Assess the morphology of the erythrocytes.
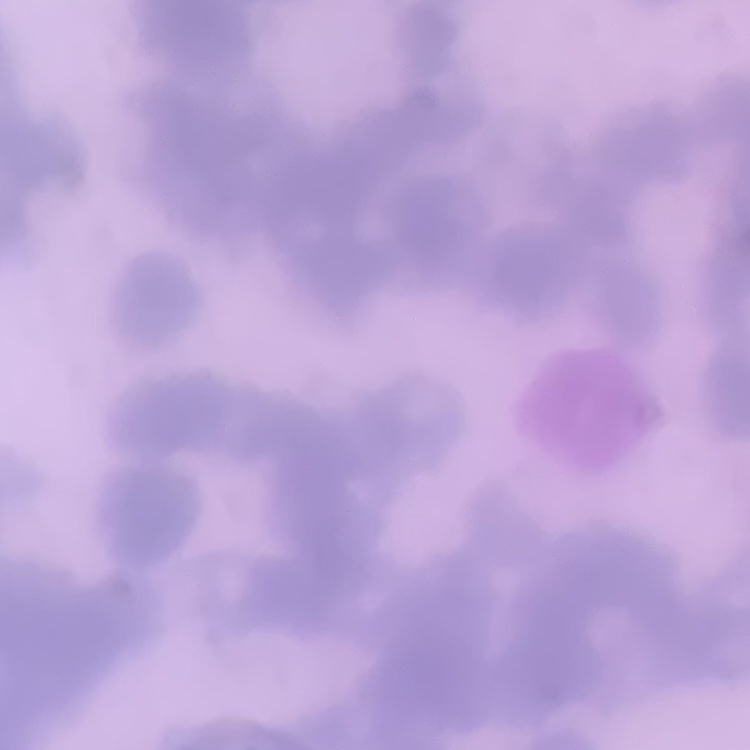
They show rouleaux formation.

Summary:
  - Preparation: thin blood film
  - Image type: square crop of a larger photomicrograph
  - Stain: Field's or Giemsa